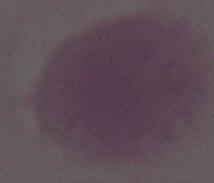

Summary:
  - Identification: erythrocyte
  - Magnification: 1000x
  - Modality: micrograph